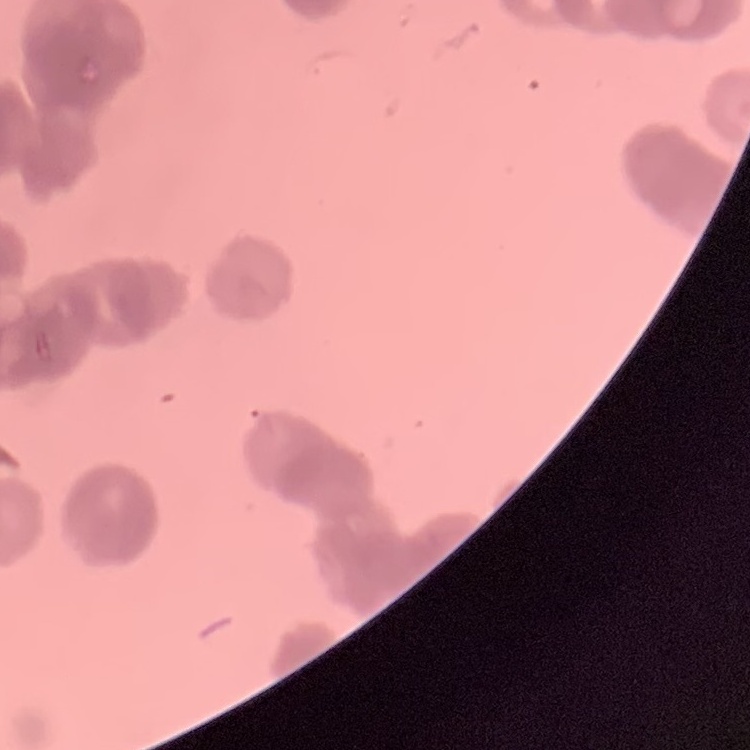

The red blood cells exhibit rouleaux formation. Stained with either Field's or Giemsa. Thin blood film. One tile cut from a larger photomicrograph.